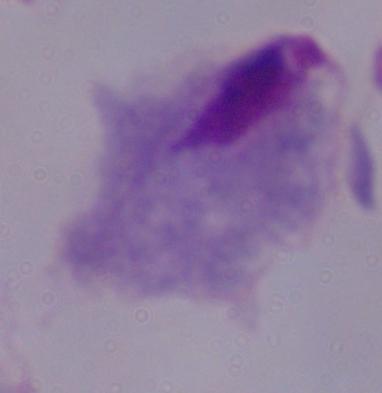

Micrograph. A trichomonad is seen. Captured at 1000x magnification.